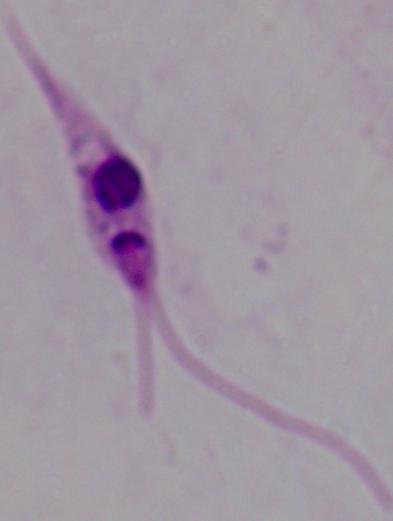
Captured at 1000x magnification. Micrograph. A Leishmania parasite is shown.